State which parasite is depicted.
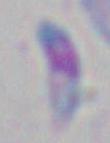
Toxoplasma gondii.

Captured at 1000x magnification. Photomicrograph.